Locate and identify every blood parasite.
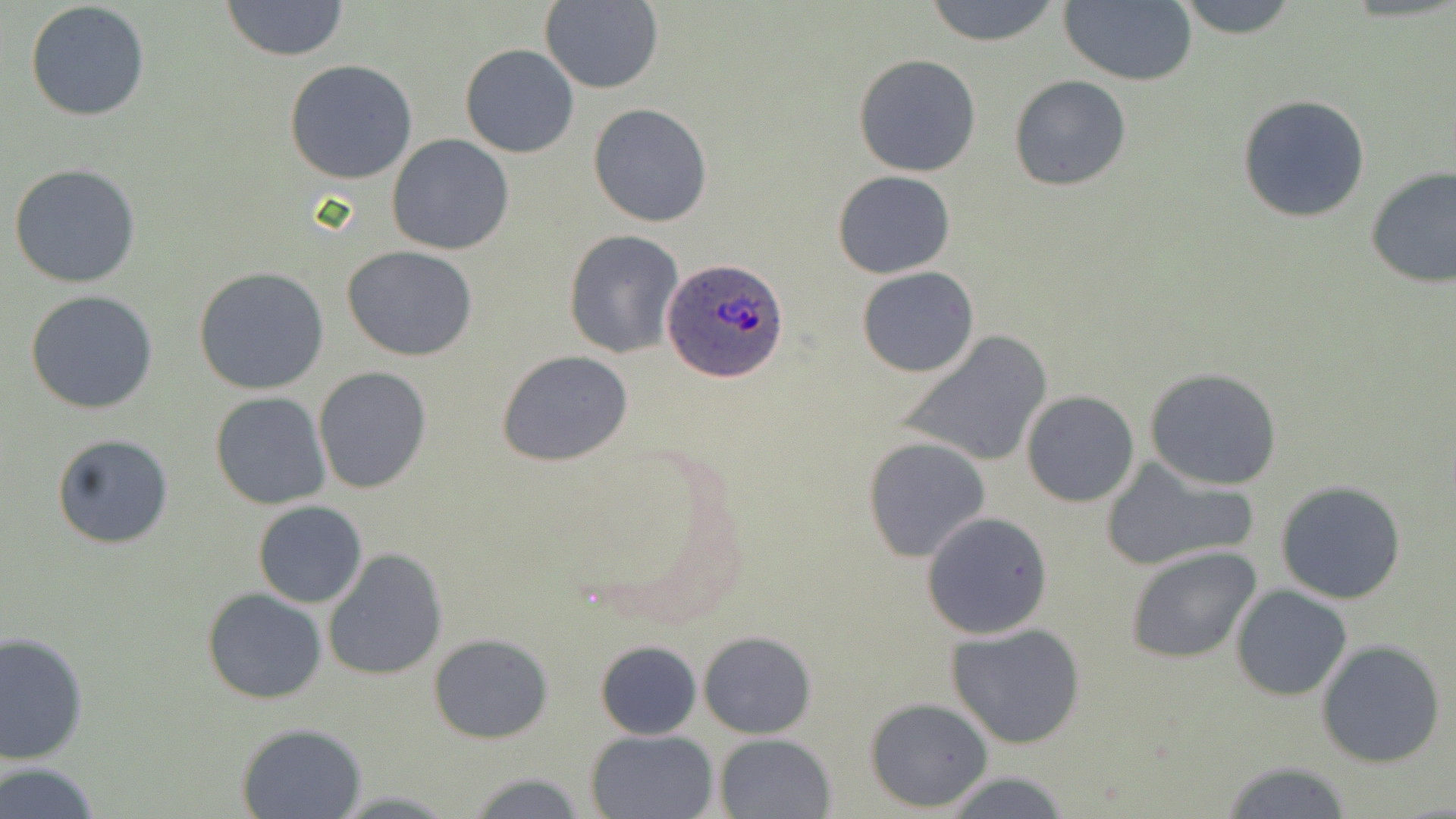
Approximate bounding boxes as [x1, y1, x2, y2] in pixels.
Plasmodium ovale-infected red blood cells: [662, 258, 790, 386].
No Plasmodium falciparum, Plasmodium malariae, Plasmodium vivax, Babesia divergens, or Trypanosoma brucei observed.

Uninfected red blood cell locations: [220, 0, 350, 63], [921, 0, 1065, 47], [1058, 0, 1197, 86], [1169, 0, 1305, 38], [25, 1, 151, 122], [538, 1, 664, 93], [460, 44, 580, 159], [854, 53, 983, 176], [284, 59, 418, 184], [1008, 75, 1131, 191], [1236, 95, 1371, 223], [588, 103, 713, 228], [386, 133, 515, 256], [8, 162, 141, 289], [1363, 165, 1456, 290], [832, 171, 955, 279], [563, 229, 684, 358], [342, 246, 480, 362], [193, 266, 330, 394], [857, 266, 980, 377], [26, 289, 158, 414], [896, 331, 1054, 470], [496, 350, 634, 466], [313, 366, 432, 496], [1144, 368, 1283, 490], [210, 391, 330, 509], [1021, 391, 1140, 507], [50, 432, 176, 551], [863, 436, 989, 564], [1100, 455, 1257, 572], [1274, 480, 1407, 604], [252, 501, 367, 608], [921, 512, 1054, 640], [1125, 544, 1261, 665], [324, 548, 448, 681], [1232, 584, 1352, 701], [202, 588, 328, 703], [947, 624, 1087, 751], [699, 630, 817, 738], [0, 632, 89, 764], [430, 634, 553, 743], [1315, 639, 1447, 769], [596, 640, 701, 739], [865, 698, 993, 813], [236, 722, 369, 818], [584, 729, 718, 818], [715, 733, 837, 819], [1219, 759, 1354, 818], [0, 761, 104, 819], [461, 772, 593, 818], [941, 772, 1072, 817]. Slide-level diagnosis: Plasmodium ovale. Image is 1456×819 pixels. Light microscopy. Captured at 1000x magnification. Thin blood smear. May-Grünwald-Giemsa stain. One field of a larger specimen.